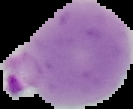

Summary:
  - Preparation: thin blood smear
  - Image size: 133×109 pixels
  - Image type: cell region segmented out of the field of view; surrounding area masked to black
  - Result: Plasmodium parasites detected